State which parasite is depicted.
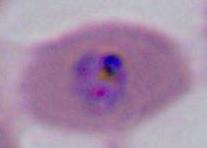

This is Plasmodium.

Captured at either 400x or 1000x magnification. Photomicrograph.